Classify this cell by malaria status.
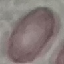

It is uninfected.

Summary:
  - Image type: cell patch, automatically extracted from a larger field of view and resized to 64 × 64 pixels
  - Stain: Giemsa
  - Preparation: thin blood film
  - Capture: smartphone camera at the microscope eyepiece